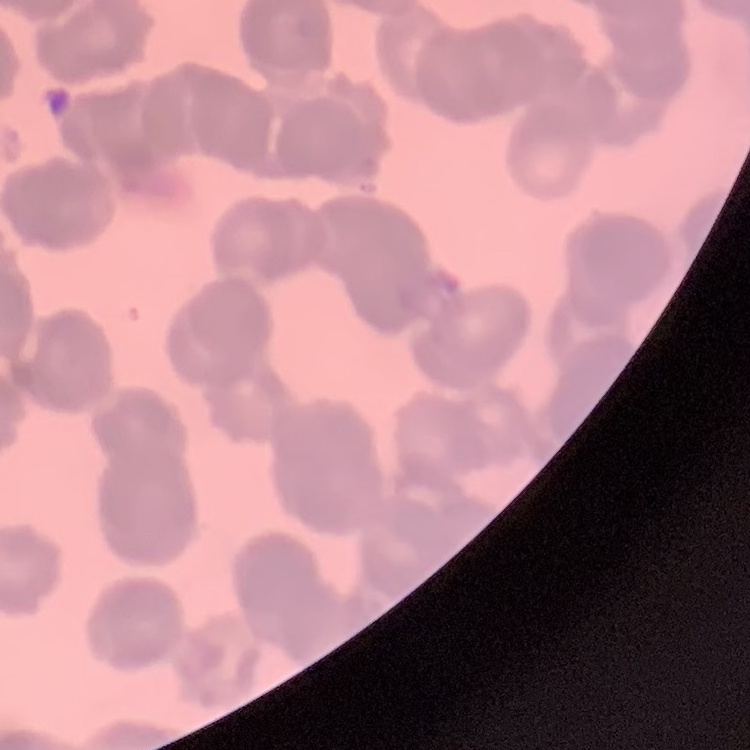
The red blood cells exhibit rouleaux formation. Thin peripheral smear. One tile cut from a larger photomicrograph. Field's or Giemsa stain.